Assess the morphology of the erythrocytes.
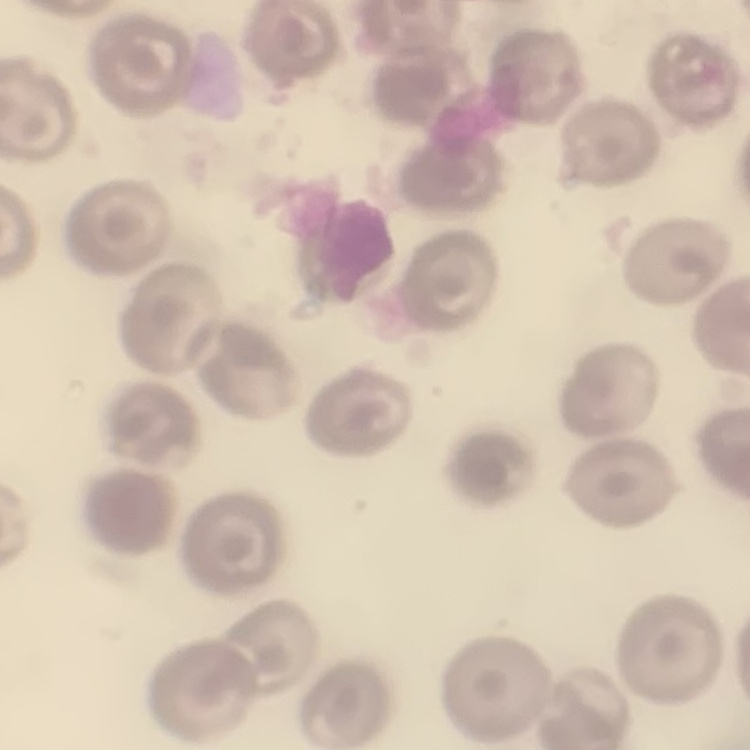
They show no rouleaux formation.

{
  "stain": "Field's or Giemsa",
  "preparation": "thin blood smear",
  "image_type": "square crop of a larger photomicrograph"
}